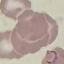

Summary:
  - Result: malaria parasites identified
  - Capture: smartphone through the microscope eyepiece
  - Stain: Giemsa
  - Image type: automatically extracted cell patch, resized to 64 × 64 pixels
  - Preparation: thin blood smear